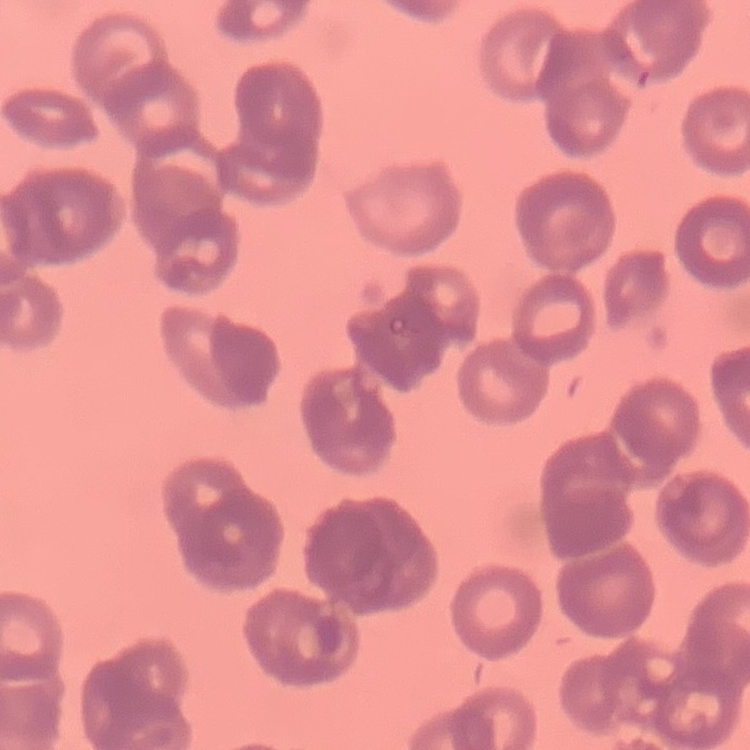

The red blood cells show rouleaux formation. Field's or Giemsa stain. Thin peripheral smear. Square crop of a larger photomicrograph.